Assess this cell for malaria.
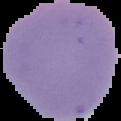
It is uninfected.

Summary:
  - Image size: 121×121 pixels
  - Image type: segmented cell region on a black background
  - Preparation: thin blood film